Assess this cell for malaria.
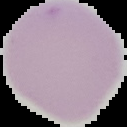
Uninfected.

From a thin blood film. Image is 127×127 pixels. Cell region segmented out of the field of view; the surrounding area is masked to black.